Give the position of every P. falciparum parasite, noting its life-cycle stage.
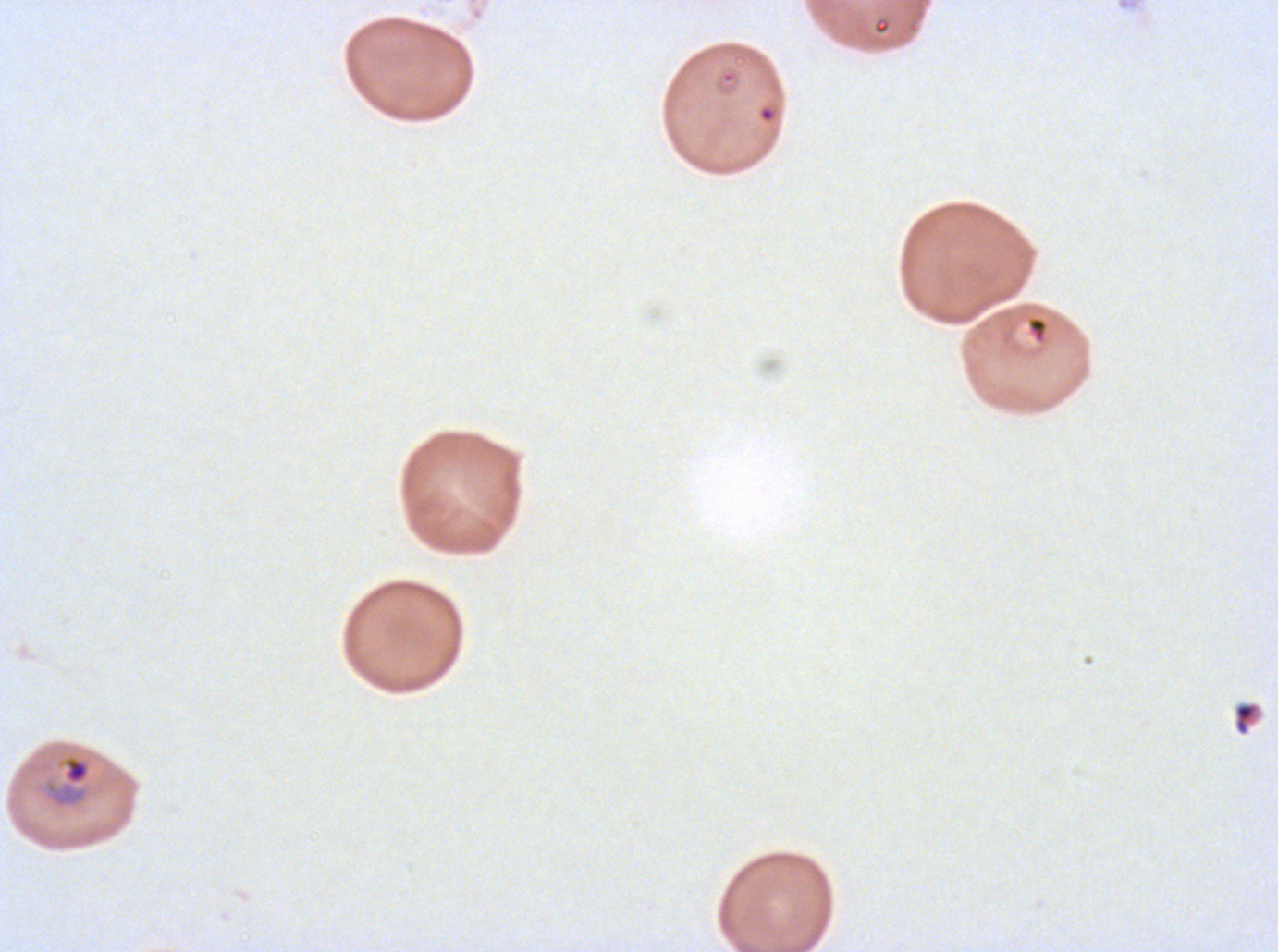

Approximate bounding rectangles given as corner coordinates in pixels from the top-left.
Rings: (x1=719, y1=68, x2=739, y2=85), (x1=1027, y1=316, x2=1048, y2=342).
Mid trophozoites: (x1=43, y1=752, x2=92, y2=811).
No late-ring/early-trophozoite forms, late trophozoites, early schizonts, late schizonts, segmenters, or gametocytes observed.

Summary:
  - Debris locations: (x1=872, y1=18, x2=891, y2=35)
  - Specimen: ex-vivo P. falciparum culture from a patient in The Gambia, grown for 24 to 48 hours
  - Stain: Giemsa
  - Preparation: thin blood film
  - Field of view: sub-image separated from a larger composite
  - Image size: 1278×952 pixels
  - Life-cycle stages observed: ring, mid trophozoite